Describe the morphology of the red blood cells.
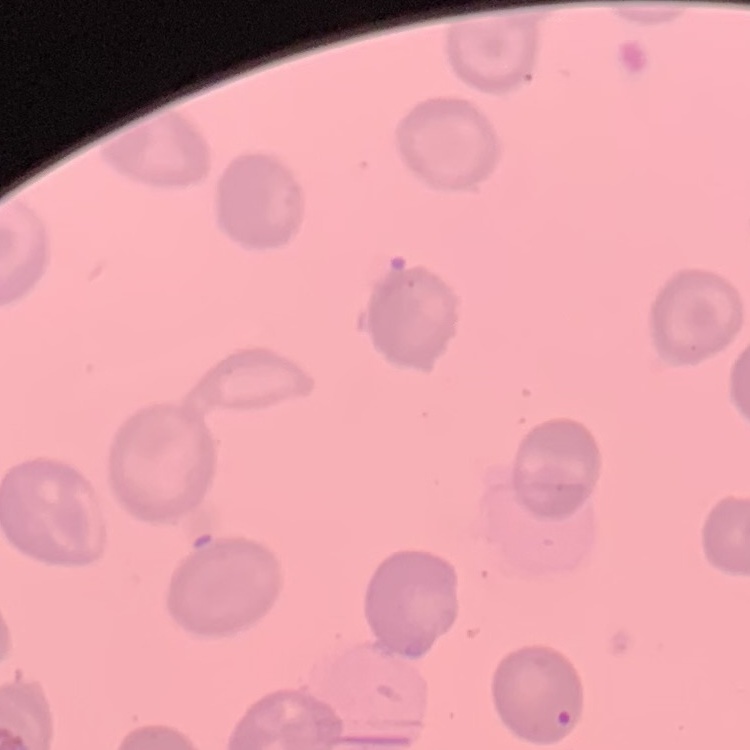

They show no rouleaux formation.

Summary:
  - Preparation: thin blood smear
  - Image type: square crop of a larger photomicrograph
  - Stain: Field's or Giemsa